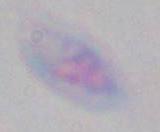 Micrograph. 1000x magnification. Toxoplasma gondii is seen.